Locate every uninfected red blood cell.
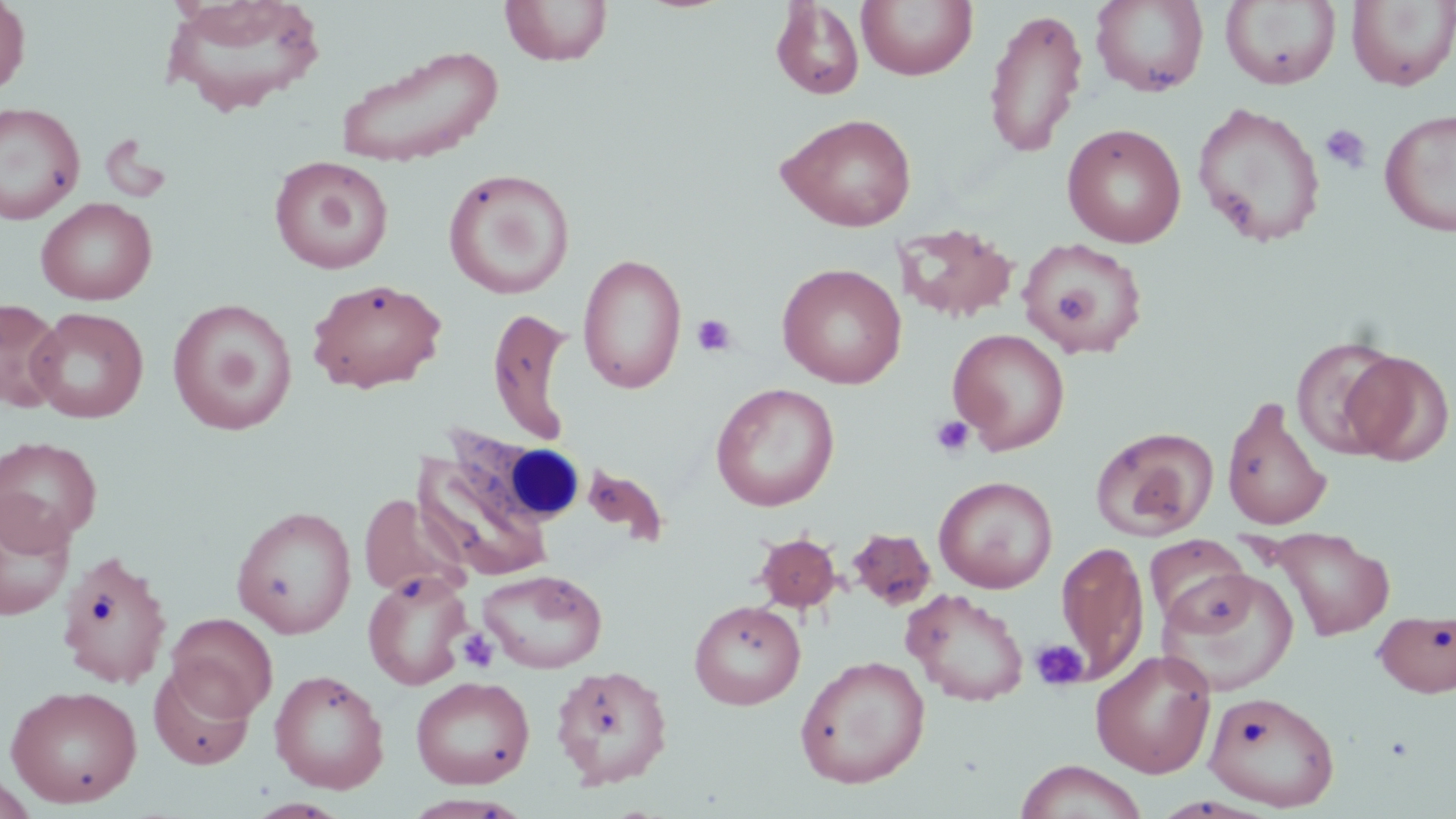

Approximate bounding boxes as [x1, y1, x2, y2] in pixels.
Uninfected red blood cells: [0, 0, 31, 96], [158, 0, 327, 117], [1091, 0, 1210, 97], [501, 1, 613, 67], [771, 1, 865, 100], [857, 1, 978, 81], [1221, 1, 1341, 89], [1347, 1, 1456, 91], [982, 7, 1088, 159], [333, 44, 505, 167], [0, 101, 86, 225], [1192, 102, 1326, 248], [1380, 108, 1456, 237], [775, 112, 918, 232], [1062, 123, 1186, 248], [269, 155, 394, 274], [443, 167, 575, 300], [36, 197, 158, 305], [893, 222, 1019, 324], [1020, 239, 1151, 358], [577, 252, 687, 394], [777, 262, 907, 389], [307, 277, 447, 394], [0, 298, 67, 413], [167, 298, 297, 436], [483, 298, 574, 441], [27, 307, 149, 423], [948, 329, 1070, 454], [1292, 335, 1403, 460], [1342, 350, 1454, 467], [711, 382, 839, 511], [1221, 395, 1334, 532], [1091, 426, 1218, 541], [0, 436, 103, 549], [410, 455, 552, 581], [582, 462, 669, 547], [934, 476, 1058, 593], [358, 493, 470, 602], [0, 494, 75, 621], [231, 505, 357, 639], [1267, 527, 1394, 641], [846, 528, 937, 611], [753, 532, 842, 613], [1145, 534, 1251, 631], [1056, 539, 1149, 685], [57, 549, 174, 690], [478, 563, 607, 669], [1157, 567, 1298, 697], [363, 571, 472, 690], [903, 588, 1030, 706], [689, 599, 806, 710], [1374, 610, 1456, 697], [166, 612, 278, 721], [1090, 649, 1217, 778], [794, 654, 931, 788], [148, 662, 256, 770], [551, 664, 674, 789], [269, 669, 390, 794], [410, 675, 535, 789], [5, 684, 143, 808], [1203, 690, 1340, 811], [1015, 760, 1149, 819], [0, 771, 39, 818].

slide-level diagnosis = no evidence of blood parasites
stain = May-Grünwald-Giemsa
image size = 1456×819 pixels
modality = optical microscopy
magnification = 1000x
field of view = single
white blood cell locations = approximate bounding boxes as [x1, y1, x2, y2] in pixels: [445, 424, 577, 529]
preparation = thin blood smear
platelet locations = approximate bounding boxes as [x1, y1, x2, y2] in pixels: [1321, 124, 1371, 173], [1053, 288, 1095, 322], [692, 314, 737, 357], [930, 415, 975, 458], [457, 629, 498, 673], [1029, 638, 1089, 692]